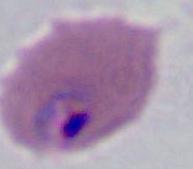

{
  "modality": "micrograph",
  "magnification": "400x or 1000x",
  "identification": "Plasmodium"
}